State the blood parasite species.
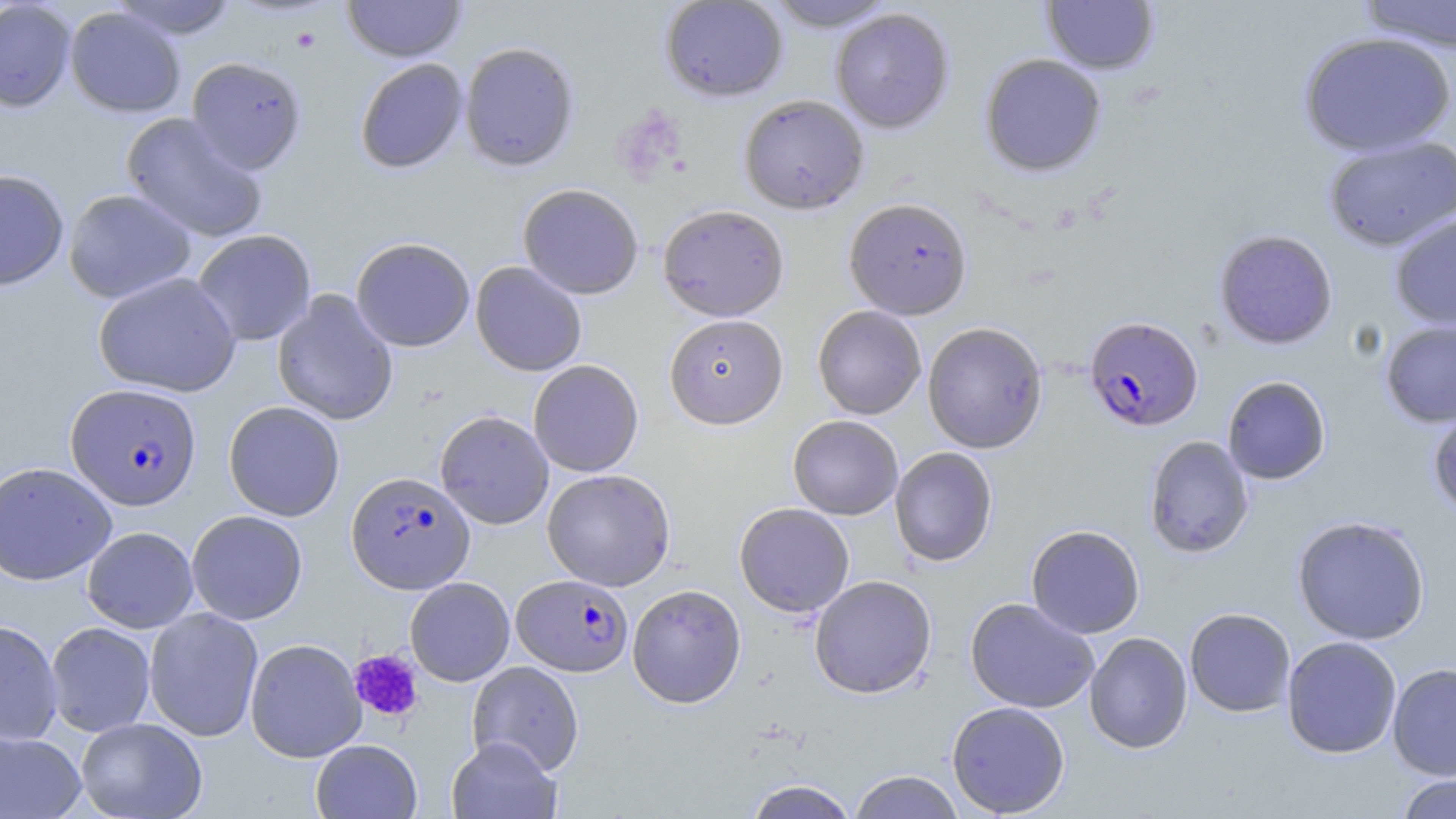

Plasmodium falciparum.

Approximate bounding boxes as (x1,y1)-(x2,y2) corner pairs in pixels. Plasmodium falciparum-infected red blood cell locations: (1083,315)-(1203,433), (66,383)-(202,510), (346,471)-(475,594), (512,575)-(633,677). Platelet locations: (349,649)-(424,723). Uninfected red blood cell locations: (110,0)-(239,41), (341,0)-(467,63), (660,0)-(788,102), (764,0)-(898,31), (1355,0)-(1456,52), (0,1)-(76,112), (1042,1)-(1159,75), (65,6)-(186,118), (830,8)-(955,134), (1297,31)-(1455,157), (459,41)-(580,172), (979,54)-(1107,177), (186,56)-(307,175), (354,58)-(468,174), (739,94)-(869,214), (121,112)-(267,244), (1323,136)-(1456,251), (0,169)-(69,292), (517,183)-(644,300), (63,188)-(197,304), (844,198)-(973,320), (657,204)-(790,322), (1390,214)-(1456,330), (192,229)-(317,345), (1213,229)-(1338,350), (351,237)-(475,352), (354,249)-(589,360), (470,261)-(587,376), (93,272)-(241,397), (272,290)-(398,426), (813,305)-(926,419), (664,314)-(788,429), (1380,318)-(1456,428), (922,321)-(1048,454), (528,360)-(644,477), (1222,376)-(1331,485), (224,401)-(345,521), (1428,404)-(1456,518), (435,410)-(554,530), (788,415)-(904,520), (1144,436)-(1254,558), (889,447)-(998,567), (0,462)-(117,585), (542,469)-(676,591), (734,503)-(855,617), (186,510)-(308,625), (1292,515)-(1431,645), (1026,524)-(1145,638), (82,527)-(198,633), (809,575)-(937,699), (405,577)-(515,686), (627,584)-(746,708), (965,597)-(1099,713), (144,607)-(264,742), (1184,607)-(1296,716), (0,620)-(63,746), (45,622)-(156,737), (1084,632)-(1192,754), (1281,636)-(1402,758), (245,638)-(366,762), (467,661)-(584,776), (1387,662)-(1456,780), (946,701)-(1070,817), (76,717)-(207,819), (0,731)-(86,818), (446,736)-(562,819), (311,739)-(423,818), (849,770)-(965,818), (1394,772)-(1456,818), (743,779)-(859,819). Thin blood film. Image is 1456×819 pixels. Optical microscopy. May-Grünwald-Giemsa stain. One field of a larger specimen. Captured at 1000x magnification.